Identify the parasite.
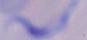
This is a trypanosome.

Photomicrograph. Captured at 1000x magnification.